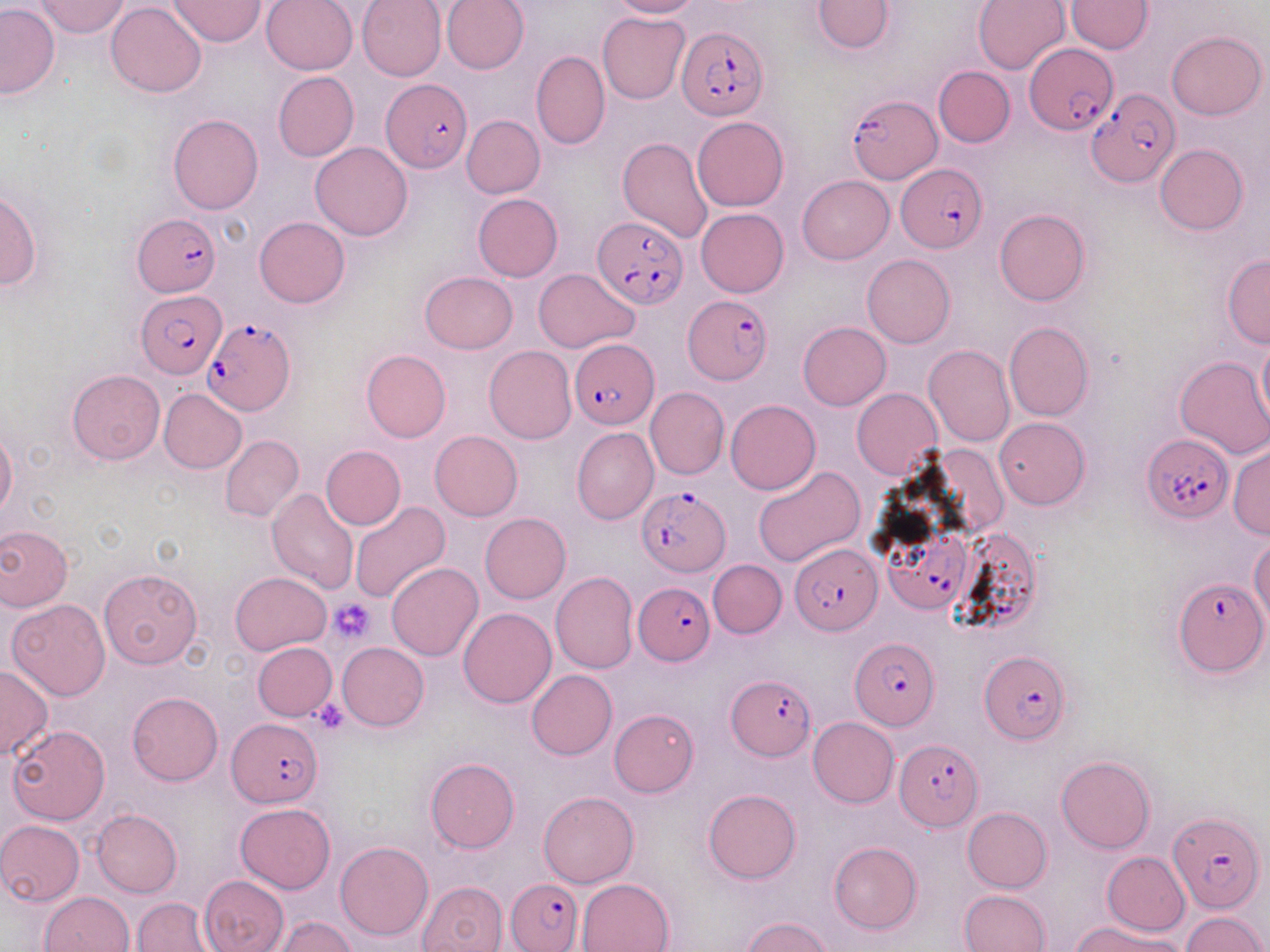
slide-level diagnosis = Plasmodium falciparum
preparation = thin blood smear
uninfected red blood cell locations = approximate bounding boxes as (x1,y1)-(x2,y2) corner pairs in pixels: (171,0)-(264,46), (260,0)-(359,75), (357,0)-(446,82), (441,0)-(529,74), (608,0)-(703,18), (812,0)-(893,53), (973,0)-(1069,73), (35,1)-(131,38), (1065,1)-(1152,54), (106,2)-(206,98), (0,4)-(59,98), (598,12)-(689,103), (1166,31)-(1266,120), (530,50)-(608,149), (933,66)-(1014,147), (273,72)-(359,162), (169,114)-(264,213), (691,114)-(789,211), (462,115)-(544,198), (618,138)-(712,242), (309,142)-(413,241), (1154,144)-(1249,235), (798,175)-(893,264), (0,189)-(43,291), (473,193)-(563,282), (696,209)-(789,296), (995,209)-(1090,306), (254,217)-(350,308), (862,252)-(955,347), (1222,253)-(1270,348), (534,268)-(639,353), (420,271)-(518,354), (1004,321)-(1094,421), (798,322)-(891,409), (1257,328)-(1270,433), (484,344)-(576,444), (923,344)-(1015,448), (361,349)-(451,443), (1174,357)-(1270,460), (68,370)-(164,465), (645,386)-(729,480), (852,388)-(942,478), (160,389)-(246,472), (725,400)-(821,495), (995,417)-(1090,509), (572,427)-(658,526), (1,428)-(18,519), (428,430)-(523,520), (220,435)-(303,523), (1228,444)-(1269,539), (320,446)-(406,530), (752,466)-(864,568), (266,488)-(360,595), (350,501)-(451,603), (480,513)-(570,603), (0,525)-(73,612), (1249,536)-(1270,632), (708,560)-(787,638), (386,562)-(483,661), (98,567)-(203,670), (550,571)-(638,674), (230,572)-(331,655), (7,598)-(110,700), (459,608)-(556,708), (252,642)-(337,721), (338,643)-(429,731), (0,665)-(53,760), (527,670)-(617,758), (128,692)-(222,786), (609,709)-(698,796), (808,717)-(899,808), (8,725)-(110,823), (1056,755)-(1155,854), (425,758)-(519,853), (703,788)-(801,884), (538,791)-(639,888), (235,804)-(335,893), (962,807)-(1052,893), (91,809)-(182,897), (0,820)-(85,904), (335,841)-(433,941), (829,842)-(923,934), (1102,851)-(1190,935), (198,875)-(288,952), (576,878)-(675,952), (418,881)-(509,952), (960,889)-(1051,952), (40,891)-(135,952), (133,897)-(216,951), (1181,912)-(1267,951), (276,915)-(356,952), (742,917)-(835,951), (1075,919)-(1182,952)
magnification = 1000x
stain = May-Grünwald-Giemsa
platelet locations = approximate bounding boxes as (x1,y1)-(x2,y2) corner pairs in pixels: (328,597)-(376,644), (312,699)-(349,734)
field of view = one of a larger specimen
image size = 1270×952 pixels
Plasmodium falciparum-infected red blood cell locations = approximate bounding boxes as (x1,y1)-(x2,y2) corner pairs in pixels: (676,27)-(768,122), (1026,47)-(1118,136), (381,79)-(473,172), (1087,88)-(1178,186), (845,93)-(942,183), (897,163)-(986,252), (133,213)-(220,295), (592,216)-(687,309), (136,291)-(225,377), (684,296)-(774,384), (205,317)-(296,417), (569,339)-(660,429), (1141,434)-(1232,524), (637,485)-(729,576), (886,526)-(971,615), (790,543)-(882,634), (1174,576)-(1269,676), (635,580)-(713,666), (849,636)-(941,729), (978,649)-(1071,744), (726,675)-(816,762), (227,718)-(323,806), (894,737)-(981,831), (1168,811)-(1265,914), (507,878)-(584,952)
modality = optical microscopy